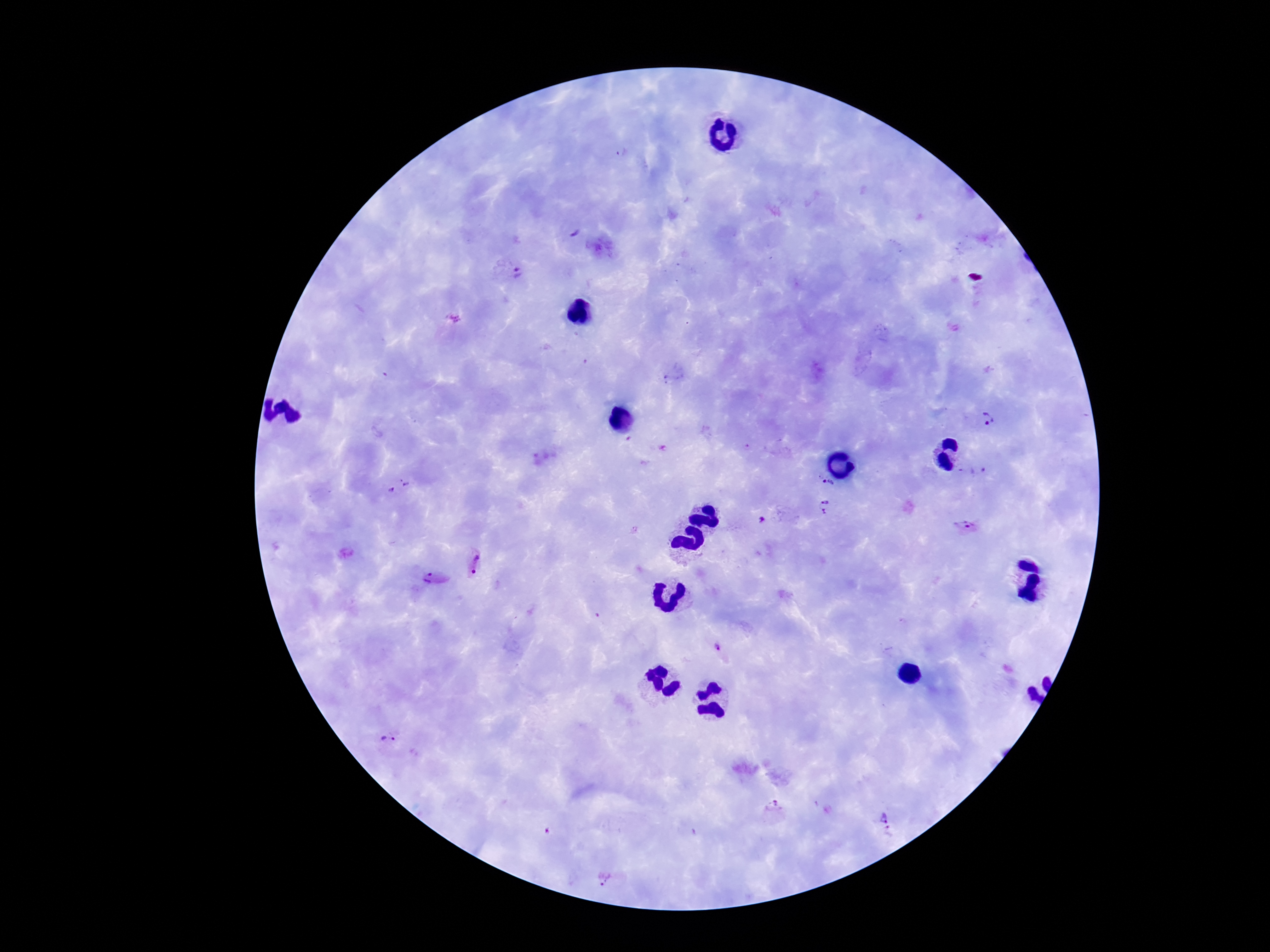

Approximate centers as [x, y] in pixels.
Summary:
  - Plasmodium parasite locations: [512, 273], [991, 421], [978, 471], [829, 484], [400, 490], [827, 506], [764, 521], [968, 527], [479, 566], [432, 582], [718, 648], [390, 743], [774, 811], [888, 823], [610, 880]
  - Preparation: thick peripheral-blood smear
  - Image size: 1270×952 pixels
  - Stain: Giemsa
  - Capture: smartphone camera through the microscope eyepiece
  - Field of view: one from this slide
  - Patient malaria status: infected
  - Magnification: 100x